Outline every Plasmodium parasite.
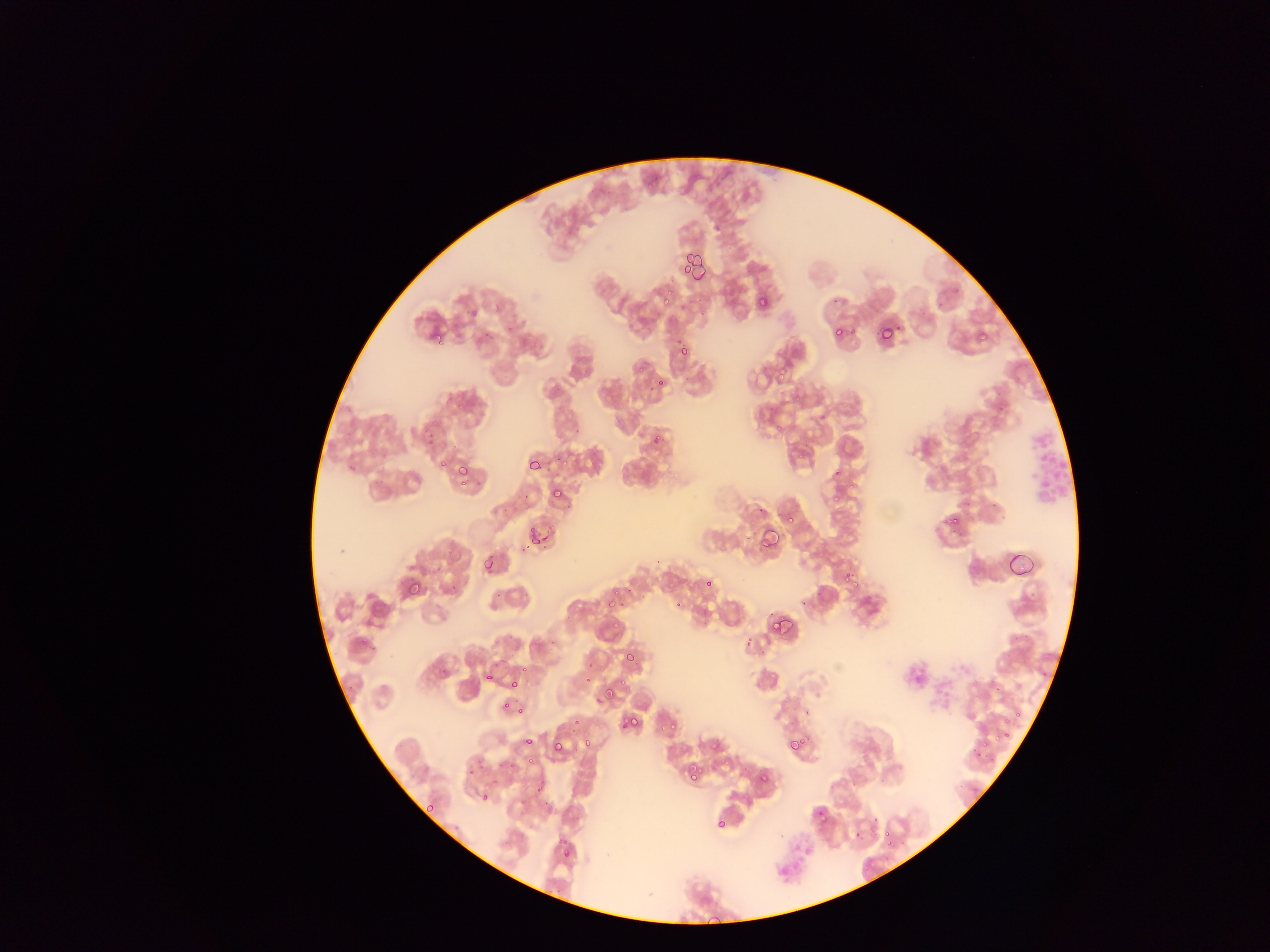
Approximate bounding boxes as (left, top, right, bottom) in pixels.
Plasmodium parasites: (668, 288, 677, 294), (756, 294, 772, 312), (662, 298, 670, 304), (876, 325, 895, 346), (426, 326, 447, 348), (679, 344, 688, 354), (639, 365, 647, 373), (777, 368, 793, 379), (658, 376, 666, 387), (457, 402, 462, 411), (773, 420, 789, 428), (427, 434, 438, 446), (652, 434, 665, 441), (459, 459, 467, 471), (436, 460, 445, 466), (347, 466, 358, 472), (460, 480, 469, 486), (828, 480, 848, 504), (549, 485, 567, 505), (778, 508, 796, 527), (943, 511, 963, 530), (527, 526, 550, 549), (760, 526, 781, 551), (481, 557, 499, 577), (701, 577, 715, 593), (402, 579, 424, 601), (675, 589, 689, 609), (605, 593, 619, 609), (769, 614, 791, 636), (624, 647, 642, 669), (521, 666, 531, 672), (478, 668, 495, 678), (583, 677, 592, 685), (598, 681, 622, 706), (510, 682, 518, 690), (501, 702, 511, 711), (998, 709, 1024, 742), (627, 716, 639, 725), (620, 718, 629, 730), (667, 720, 681, 729), (996, 720, 1016, 744), (524, 733, 534, 743), (788, 734, 810, 755), (545, 735, 580, 759), (550, 739, 568, 760), (584, 740, 590, 748), (526, 755, 534, 766), (757, 771, 772, 788), (688, 774, 696, 782), (532, 780, 543, 795), (422, 800, 436, 814), (812, 806, 831, 827), (714, 816, 729, 832), (852, 826, 867, 842), (879, 830, 896, 851), (564, 844, 575, 856) | approximate (x, y) pixel centers of objects too small to bound: (521, 711), (574, 714).

Thin blood smear. Mobile-phone photograph taken through the microscope. Image is 1270×952 pixels. Collected in Ghana. Single field of view.